Outline each blood parasite and name the species.
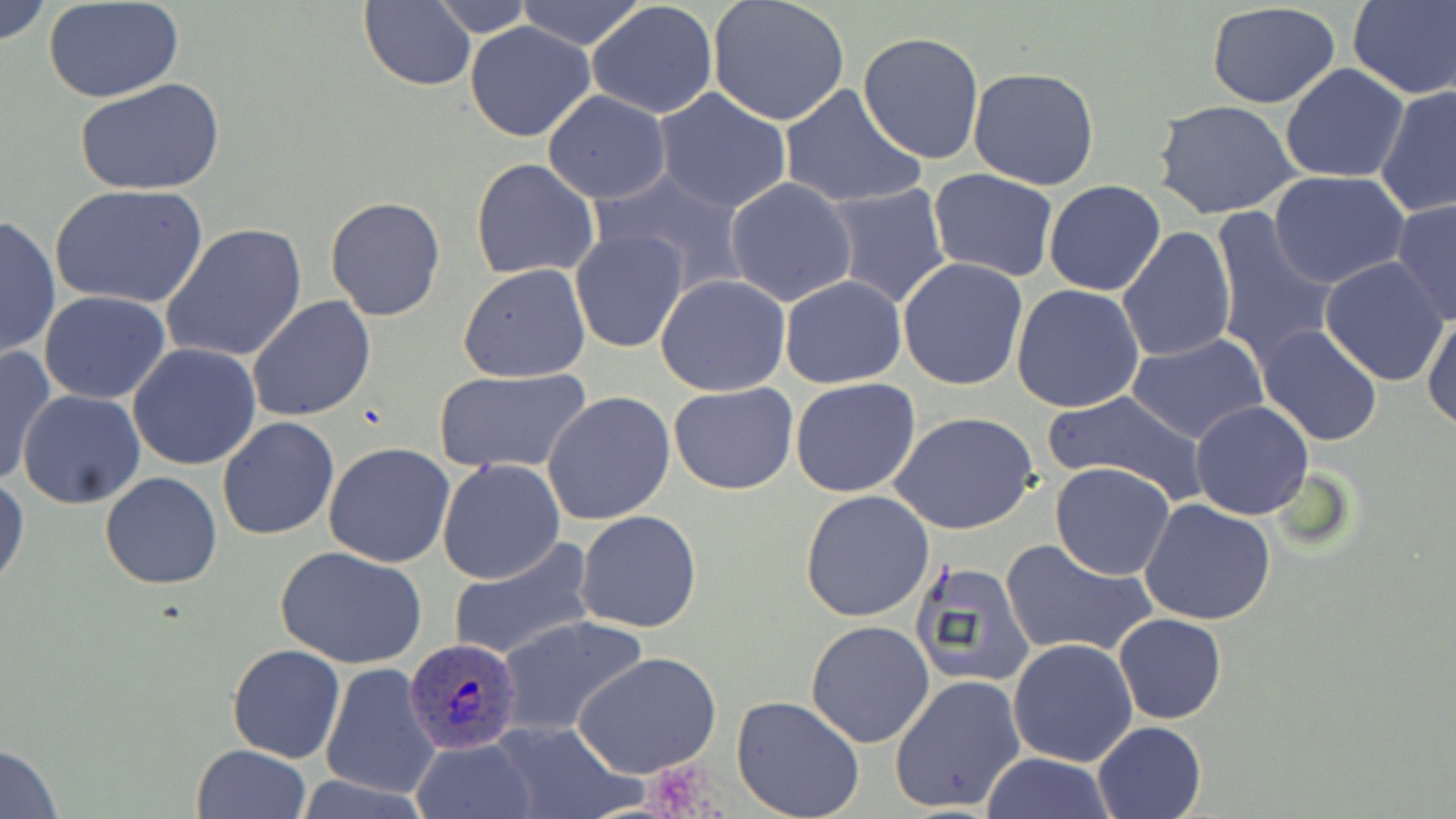
Approximate bounding boxes as named x1/y1/x2/y2 corners in pixels.
Plasmodium ovale-infected red blood cells: (x1=403, y1=637, x2=521, y2=754).
No Plasmodium falciparum, Plasmodium malariae, Plasmodium vivax, Babesia divergens, or Trypanosoma brucei observed.

slide-level diagnosis = Plasmodium ovale
stain = May-Grünwald-Giemsa
modality = light microscopy
uninfected red blood cell locations = approximate bounding boxes as named x1/y1/x2/y2 corners in pixels: (x1=1, y1=0, x2=51, y2=48), (x1=425, y1=0, x2=539, y2=36), (x1=706, y1=0, x2=851, y2=126), (x1=1348, y1=0, x2=1456, y2=100), (x1=358, y1=1, x2=478, y2=90), (x1=514, y1=1, x2=647, y2=50), (x1=588, y1=1, x2=719, y2=119), (x1=44, y1=2, x2=187, y2=103), (x1=1206, y1=3, x2=1345, y2=110), (x1=465, y1=21, x2=596, y2=141), (x1=858, y1=30, x2=985, y2=163), (x1=1280, y1=64, x2=1411, y2=183), (x1=967, y1=66, x2=1100, y2=190), (x1=74, y1=77, x2=225, y2=196), (x1=1376, y1=83, x2=1456, y2=218), (x1=779, y1=85, x2=925, y2=209), (x1=653, y1=86, x2=794, y2=214), (x1=541, y1=91, x2=671, y2=204), (x1=1153, y1=100, x2=1300, y2=220), (x1=471, y1=158, x2=600, y2=280), (x1=928, y1=168, x2=1057, y2=279), (x1=590, y1=169, x2=747, y2=296), (x1=1267, y1=171, x2=1412, y2=291), (x1=724, y1=177, x2=857, y2=306), (x1=1043, y1=180, x2=1166, y2=296), (x1=822, y1=182, x2=951, y2=307), (x1=49, y1=184, x2=209, y2=310), (x1=324, y1=196, x2=448, y2=321), (x1=1390, y1=199, x2=1456, y2=326), (x1=1209, y1=207, x2=1341, y2=369), (x1=1, y1=214, x2=60, y2=361), (x1=162, y1=222, x2=308, y2=365), (x1=1116, y1=227, x2=1236, y2=363), (x1=571, y1=230, x2=688, y2=352), (x1=896, y1=257, x2=1029, y2=392), (x1=1322, y1=258, x2=1448, y2=385), (x1=459, y1=265, x2=590, y2=383), (x1=655, y1=273, x2=791, y2=395), (x1=780, y1=274, x2=906, y2=388), (x1=1012, y1=284, x2=1145, y2=414), (x1=39, y1=291, x2=172, y2=405), (x1=247, y1=295, x2=377, y2=423), (x1=1422, y1=309, x2=1455, y2=433), (x1=1255, y1=324, x2=1383, y2=447), (x1=1128, y1=332, x2=1268, y2=446), (x1=128, y1=342, x2=261, y2=470), (x1=0, y1=344, x2=58, y2=489), (x1=432, y1=366, x2=594, y2=475), (x1=791, y1=377, x2=921, y2=498), (x1=669, y1=382, x2=799, y2=496), (x1=17, y1=390, x2=147, y2=510), (x1=542, y1=392, x2=675, y2=525), (x1=1042, y1=393, x2=1208, y2=504), (x1=1190, y1=401, x2=1313, y2=520), (x1=890, y1=412, x2=1040, y2=536), (x1=217, y1=417, x2=340, y2=540), (x1=323, y1=443, x2=456, y2=568), (x1=437, y1=458, x2=565, y2=585), (x1=1049, y1=462, x2=1175, y2=581), (x1=100, y1=471, x2=222, y2=590), (x1=1, y1=473, x2=28, y2=592), (x1=800, y1=490, x2=935, y2=623), (x1=1139, y1=498, x2=1279, y2=626), (x1=576, y1=510, x2=702, y2=634), (x1=446, y1=537, x2=596, y2=664), (x1=1001, y1=538, x2=1157, y2=660), (x1=275, y1=546, x2=427, y2=669), (x1=909, y1=560, x2=1035, y2=691), (x1=1114, y1=614, x2=1226, y2=725), (x1=494, y1=615, x2=649, y2=740), (x1=805, y1=620, x2=935, y2=748), (x1=1008, y1=638, x2=1138, y2=767), (x1=227, y1=644, x2=345, y2=763), (x1=574, y1=650, x2=722, y2=779), (x1=319, y1=663, x2=441, y2=801), (x1=890, y1=674, x2=1026, y2=814), (x1=731, y1=695, x2=865, y2=819), (x1=487, y1=720, x2=642, y2=819), (x1=1092, y1=720, x2=1206, y2=819), (x1=410, y1=737, x2=539, y2=819), (x1=0, y1=742, x2=64, y2=817), (x1=189, y1=745, x2=312, y2=819), (x1=978, y1=753, x2=1119, y2=818)
image size = 1456×819 pixels
preparation = thin blood smear
magnification = 1000x
field of view = one of a larger specimen